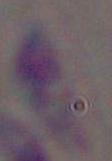
Summary:
  - Magnification: 1000x
  - Modality: photomicrograph
  - Identification: Toxoplasma gondii